Outline each Plasmodium falciparum-infected red blood cell.
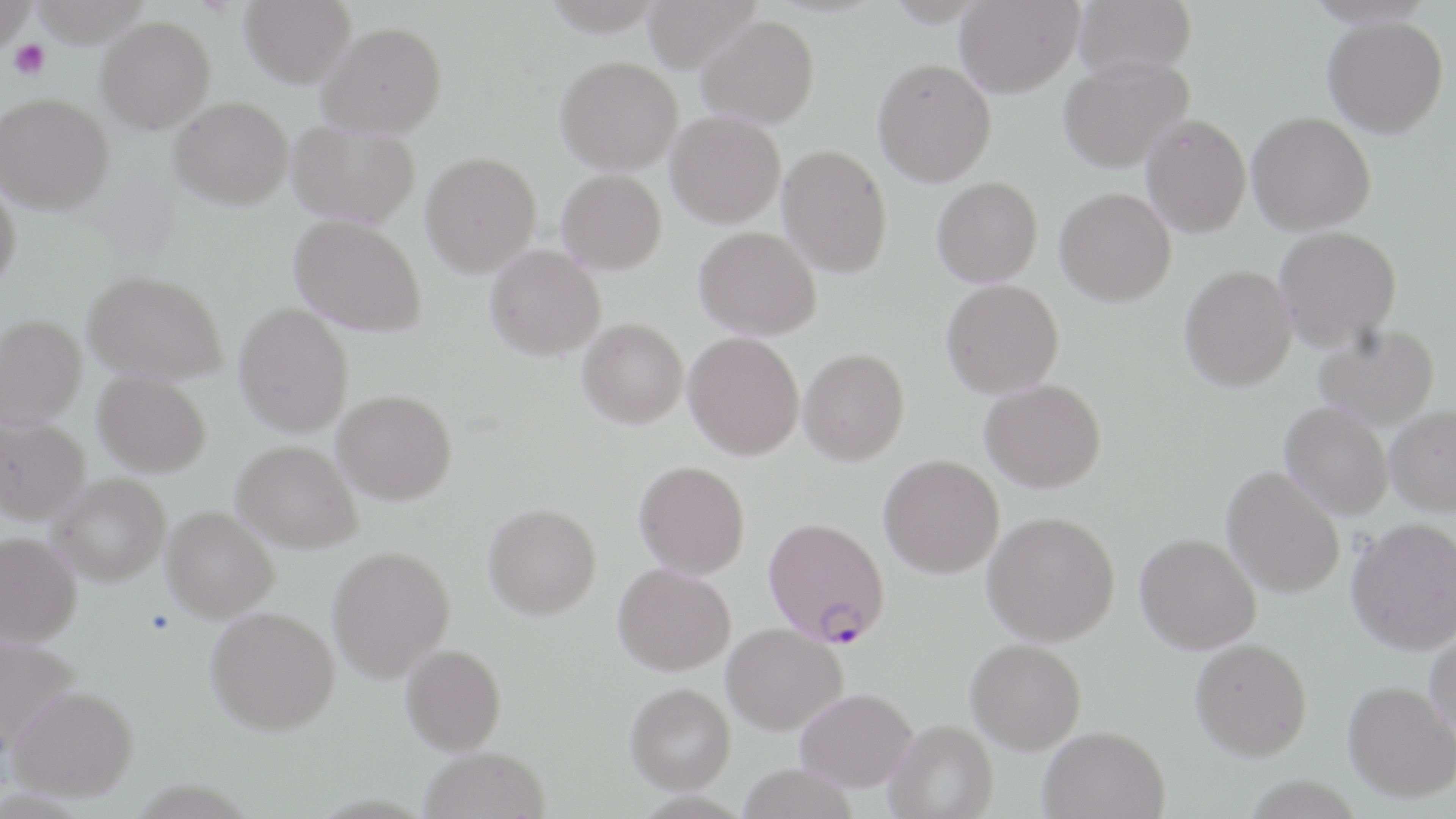

Approximate bounding boxes as named x1/y1/x2/y2 corners in pixels.
Plasmodium falciparum-infected red blood cells: (x1=763, y1=516, x2=889, y2=647).

Platelet locations: (x1=7, y1=38, x2=50, y2=80). Uninfected red blood cell locations: (x1=0, y1=0, x2=36, y2=56), (x1=240, y1=0, x2=356, y2=88), (x1=641, y1=0, x2=761, y2=73), (x1=954, y1=0, x2=1084, y2=97), (x1=1073, y1=0, x2=1196, y2=80), (x1=697, y1=15, x2=819, y2=128), (x1=96, y1=16, x2=216, y2=134), (x1=1323, y1=16, x2=1448, y2=138), (x1=317, y1=21, x2=447, y2=138), (x1=555, y1=55, x2=683, y2=174), (x1=1058, y1=56, x2=1194, y2=173), (x1=872, y1=58, x2=996, y2=187), (x1=0, y1=93, x2=114, y2=213), (x1=170, y1=96, x2=293, y2=209), (x1=666, y1=110, x2=786, y2=227), (x1=1247, y1=111, x2=1376, y2=234), (x1=1141, y1=114, x2=1251, y2=238), (x1=288, y1=121, x2=420, y2=227), (x1=778, y1=144, x2=891, y2=278), (x1=421, y1=151, x2=541, y2=276), (x1=557, y1=169, x2=666, y2=274), (x1=932, y1=177, x2=1043, y2=287), (x1=0, y1=181, x2=20, y2=291), (x1=1055, y1=187, x2=1176, y2=306), (x1=290, y1=214, x2=428, y2=337), (x1=1273, y1=225, x2=1402, y2=351), (x1=695, y1=226, x2=821, y2=340), (x1=485, y1=244, x2=605, y2=359), (x1=1179, y1=264, x2=1297, y2=391), (x1=83, y1=270, x2=227, y2=383), (x1=941, y1=279, x2=1063, y2=398), (x1=234, y1=303, x2=353, y2=437), (x1=1, y1=315, x2=86, y2=428), (x1=578, y1=318, x2=688, y2=428), (x1=1313, y1=324, x2=1440, y2=430), (x1=684, y1=332, x2=804, y2=460), (x1=799, y1=349, x2=909, y2=465), (x1=94, y1=370, x2=211, y2=476), (x1=980, y1=379, x2=1106, y2=492), (x1=332, y1=390, x2=457, y2=504), (x1=1281, y1=402, x2=1393, y2=519), (x1=1385, y1=404, x2=1456, y2=515), (x1=0, y1=416, x2=90, y2=524), (x1=232, y1=440, x2=362, y2=552), (x1=879, y1=455, x2=1003, y2=578), (x1=634, y1=460, x2=750, y2=579), (x1=1222, y1=466, x2=1345, y2=598), (x1=49, y1=473, x2=170, y2=585), (x1=483, y1=503, x2=601, y2=619), (x1=161, y1=506, x2=279, y2=622), (x1=983, y1=511, x2=1119, y2=645), (x1=1346, y1=517, x2=1456, y2=654), (x1=0, y1=531, x2=81, y2=646), (x1=1135, y1=533, x2=1261, y2=654), (x1=328, y1=545, x2=455, y2=682), (x1=613, y1=563, x2=735, y2=675), (x1=205, y1=606, x2=339, y2=735), (x1=722, y1=622, x2=847, y2=735), (x1=1426, y1=622, x2=1456, y2=747), (x1=0, y1=633, x2=81, y2=748), (x1=1190, y1=638, x2=1312, y2=760), (x1=966, y1=639, x2=1086, y2=753), (x1=401, y1=644, x2=506, y2=755), (x1=1343, y1=681, x2=1455, y2=801), (x1=626, y1=683, x2=735, y2=794), (x1=7, y1=684, x2=138, y2=800), (x1=796, y1=687, x2=917, y2=792), (x1=885, y1=720, x2=998, y2=819), (x1=1039, y1=726, x2=1171, y2=818), (x1=419, y1=746, x2=551, y2=819), (x1=737, y1=764, x2=858, y2=819). Slide-level diagnosis: Plasmodium falciparum. Thin blood smear. Single field of view. Captured at 1000x magnification. Image is 1456×819 pixels. Light microscopy. May-Grünwald-Giemsa-stained preparation.